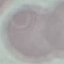
Result: negative for malaria parasites. Thin blood smear. Photographed with a smartphone camera at the microscope eyepiece. Giemsa stain. Cell patch, automatically extracted from a larger field of view and resized to 64 × 64 pixels.